Outline each uninfected red blood cell.
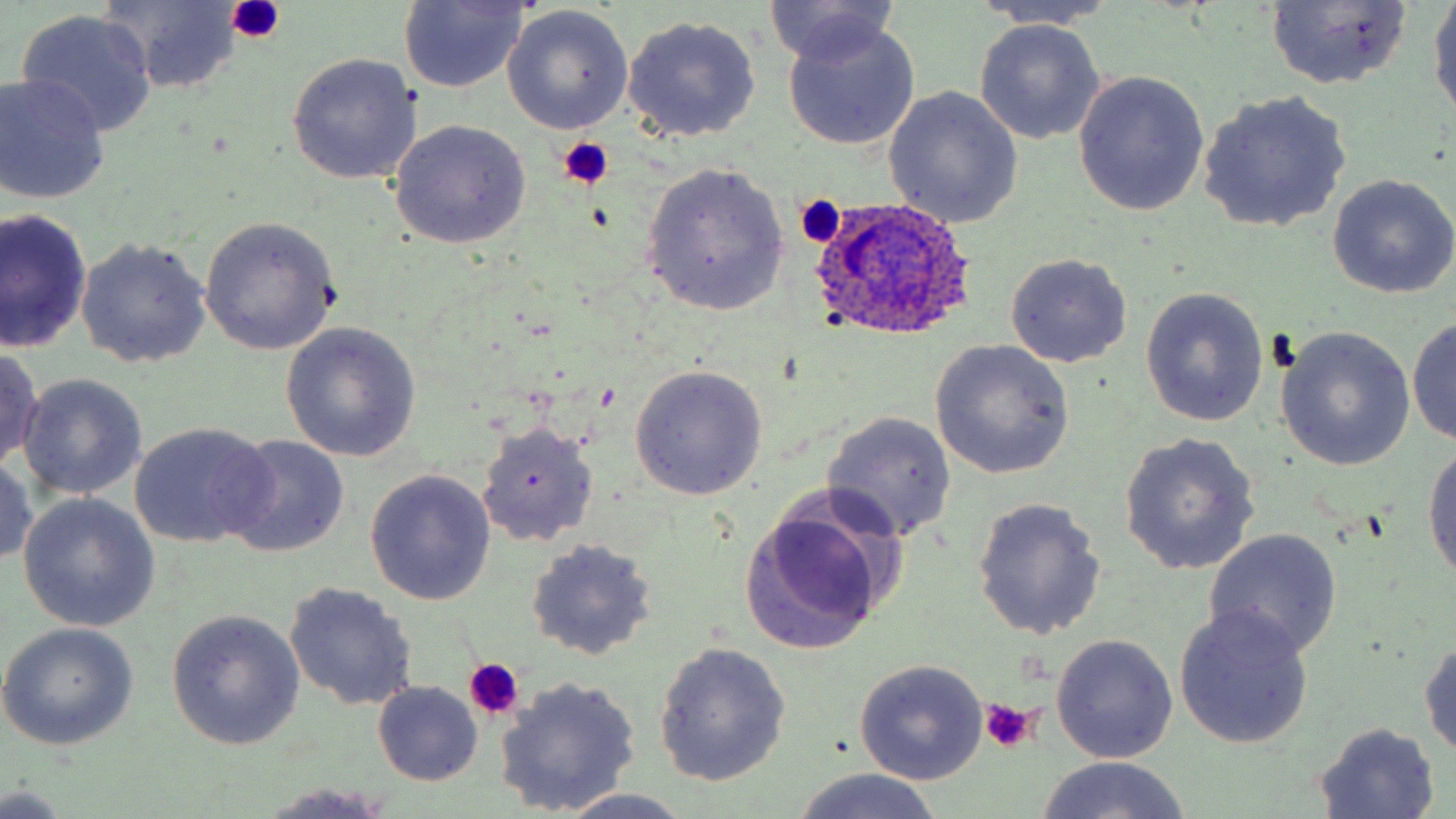

Approximate bounding boxes as named x1/y1/x2/y2 corners in pixels.
Uninfected red blood cells: (x1=1429, y1=0, x2=1456, y2=122), (x1=398, y1=1, x2=529, y2=93), (x1=765, y1=1, x2=903, y2=70), (x1=98, y1=2, x2=248, y2=90), (x1=971, y1=2, x2=1122, y2=31), (x1=1266, y1=2, x2=1413, y2=90), (x1=504, y1=7, x2=635, y2=134), (x1=16, y1=10, x2=158, y2=136), (x1=621, y1=14, x2=762, y2=142), (x1=781, y1=17, x2=921, y2=152), (x1=975, y1=19, x2=1107, y2=144), (x1=285, y1=53, x2=422, y2=186), (x1=1072, y1=72, x2=1208, y2=216), (x1=0, y1=73, x2=112, y2=204), (x1=883, y1=87, x2=1024, y2=229), (x1=1199, y1=90, x2=1354, y2=234), (x1=388, y1=119, x2=531, y2=249), (x1=641, y1=161, x2=791, y2=315), (x1=1326, y1=174, x2=1456, y2=299), (x1=1, y1=209, x2=92, y2=354), (x1=198, y1=217, x2=339, y2=354), (x1=76, y1=237, x2=211, y2=367), (x1=1005, y1=253, x2=1133, y2=369), (x1=1141, y1=287, x2=1269, y2=428), (x1=1407, y1=316, x2=1456, y2=445), (x1=281, y1=322, x2=423, y2=464), (x1=1275, y1=327, x2=1416, y2=472), (x1=930, y1=340, x2=1074, y2=479), (x1=0, y1=347, x2=45, y2=470), (x1=629, y1=365, x2=768, y2=501), (x1=18, y1=374, x2=146, y2=501), (x1=822, y1=412, x2=957, y2=542), (x1=130, y1=422, x2=276, y2=548), (x1=476, y1=422, x2=599, y2=547), (x1=1119, y1=433, x2=1261, y2=575), (x1=221, y1=436, x2=351, y2=557), (x1=1422, y1=439, x2=1456, y2=595), (x1=0, y1=452, x2=38, y2=568), (x1=365, y1=470, x2=497, y2=606), (x1=19, y1=493, x2=158, y2=632), (x1=971, y1=497, x2=1107, y2=639), (x1=739, y1=501, x2=895, y2=654), (x1=1204, y1=527, x2=1343, y2=660), (x1=526, y1=538, x2=658, y2=660), (x1=285, y1=582, x2=419, y2=711), (x1=1173, y1=605, x2=1315, y2=750), (x1=167, y1=611, x2=304, y2=749), (x1=0, y1=623, x2=140, y2=751), (x1=1051, y1=634, x2=1179, y2=763), (x1=1419, y1=635, x2=1456, y2=765), (x1=655, y1=641, x2=791, y2=785), (x1=853, y1=661, x2=988, y2=785), (x1=495, y1=675, x2=643, y2=816), (x1=373, y1=682, x2=482, y2=785), (x1=1312, y1=723, x2=1443, y2=816), (x1=1035, y1=756, x2=1195, y2=819), (x1=789, y1=768, x2=947, y2=819), (x1=0, y1=784, x2=72, y2=816), (x1=261, y1=784, x2=398, y2=817), (x1=547, y1=790, x2=699, y2=819).

Platelet locations: (x1=226, y1=0, x2=286, y2=42), (x1=558, y1=137, x2=615, y2=190), (x1=796, y1=194, x2=847, y2=248), (x1=463, y1=659, x2=526, y2=721), (x1=977, y1=700, x2=1042, y2=756). Plasmodium ovale-infected red blood cell locations: (x1=808, y1=196, x2=977, y2=341). Slide-level diagnosis: Plasmodium ovale. One field of a larger specimen. May-Grünwald-Giemsa-stained preparation. Thin blood smear. Captured at 1000x magnification. Light microscopy. Image is 1456×819 pixels.